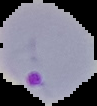

preparation = thin blood smear
image size = 97×106 pixels
malaria status = parasitized
image type = cell region segmented out of the field of view; surrounding area masked to black